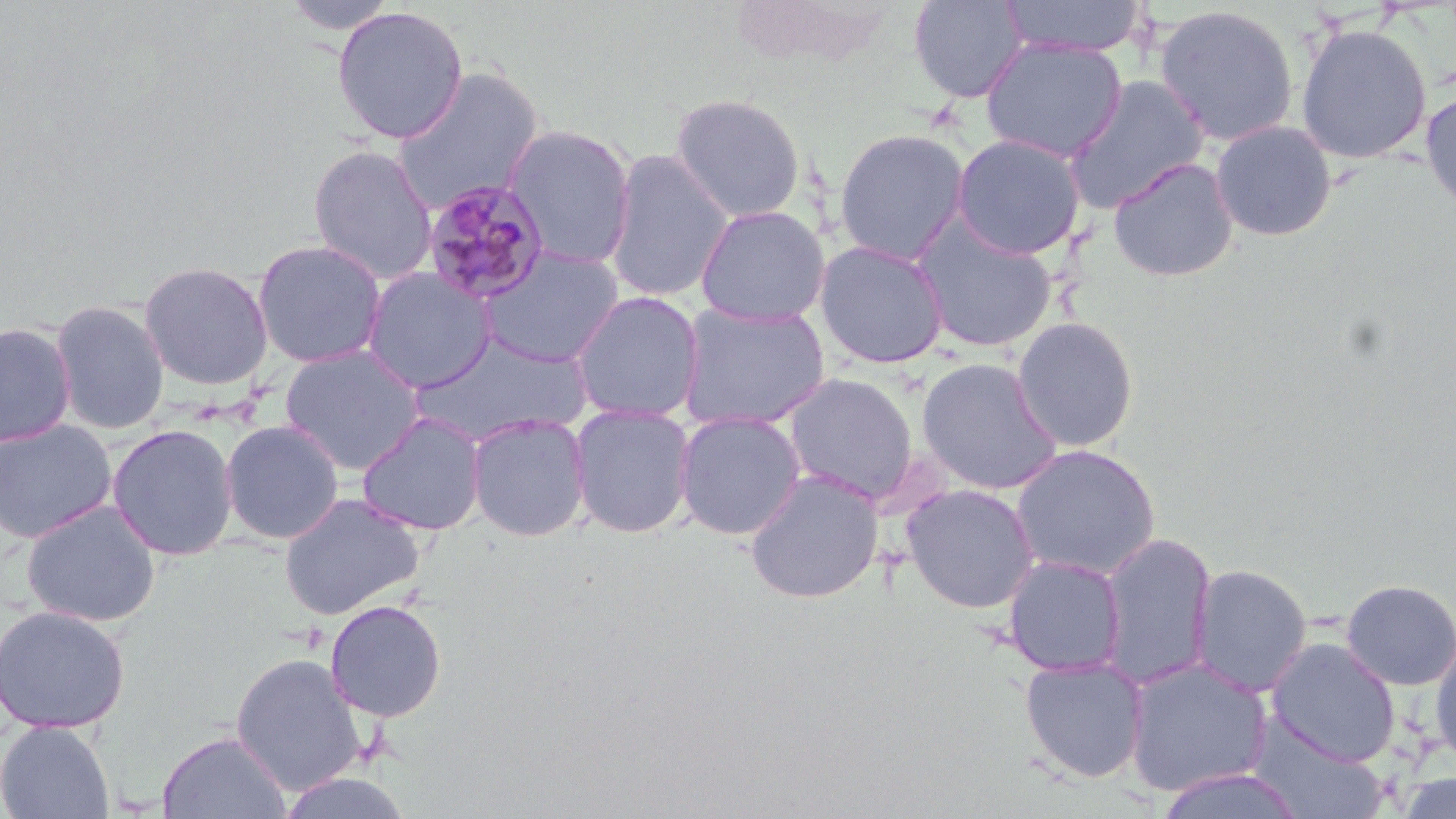
Summary:
  - Coordinate format: approximate bounding boxes as [x1, y1, x2, y2] in pixels
  - Plasmodium malariae-infected red blood cell locations: [420, 180, 551, 305]
  - Uninfected red blood cell locations: [280, 0, 401, 36], [908, 0, 1029, 103], [998, 0, 1148, 58], [1154, 5, 1300, 147], [331, 6, 469, 144], [1295, 23, 1432, 164], [981, 38, 1127, 162], [391, 66, 545, 214], [1063, 74, 1211, 213], [1421, 88, 1456, 215], [670, 92, 806, 223], [1210, 120, 1337, 241], [502, 123, 637, 269], [834, 128, 970, 265], [950, 133, 1086, 260], [307, 143, 439, 286], [604, 150, 735, 303], [1108, 157, 1239, 282], [695, 205, 831, 326], [911, 216, 1058, 353], [252, 239, 388, 368], [814, 240, 949, 369], [476, 246, 624, 367], [137, 260, 274, 391], [363, 267, 496, 394], [569, 290, 705, 424], [50, 299, 170, 435], [677, 302, 830, 432], [1010, 316, 1140, 453], [0, 322, 76, 447], [413, 335, 592, 445], [278, 344, 427, 476], [915, 357, 1064, 495], [782, 372, 920, 505], [569, 403, 697, 539], [674, 410, 806, 540], [356, 412, 488, 536], [466, 413, 591, 542], [0, 418, 117, 544], [220, 419, 344, 544], [107, 423, 238, 561], [1010, 444, 1161, 581], [744, 470, 884, 604], [902, 483, 1040, 613], [278, 493, 425, 621], [21, 499, 162, 627], [1097, 532, 1218, 690], [1002, 553, 1127, 678], [1189, 563, 1313, 697], [1340, 578, 1456, 690], [324, 599, 447, 722], [0, 604, 131, 733], [1266, 637, 1401, 766], [1430, 637, 1456, 769], [230, 651, 368, 796], [1019, 656, 1149, 783], [1123, 658, 1274, 799], [1244, 714, 1391, 819], [0, 719, 116, 819], [158, 730, 291, 819], [1154, 768, 1307, 819], [276, 772, 414, 819]
  - Slide-level diagnosis: Plasmodium malariae
  - Preparation: thin blood smear
  - Stain: May-Grünwald-Giemsa
  - Image size: 1456×819 pixels
  - Magnification: 1000x
  - Field of view: one of a larger specimen
  - Modality: light microscopy